Classify this cell by malaria status.
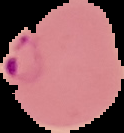

It is parasitized.

preparation: thin blood film
image_size: 124×133 pixels
image_type: segmented cell region with the area outside set to black